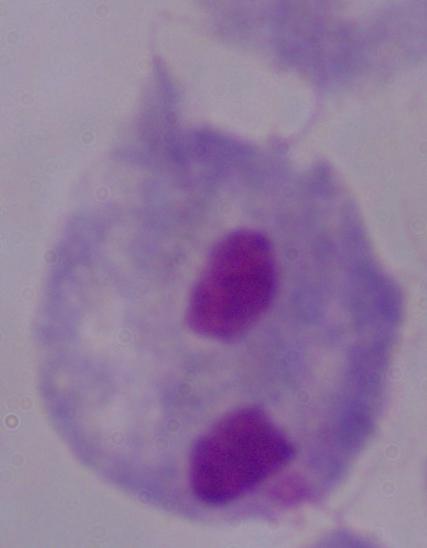
{
  "identification": "trichomonad",
  "modality": "micrograph",
  "magnification": "1000x"
}